Name the blood parasite species.
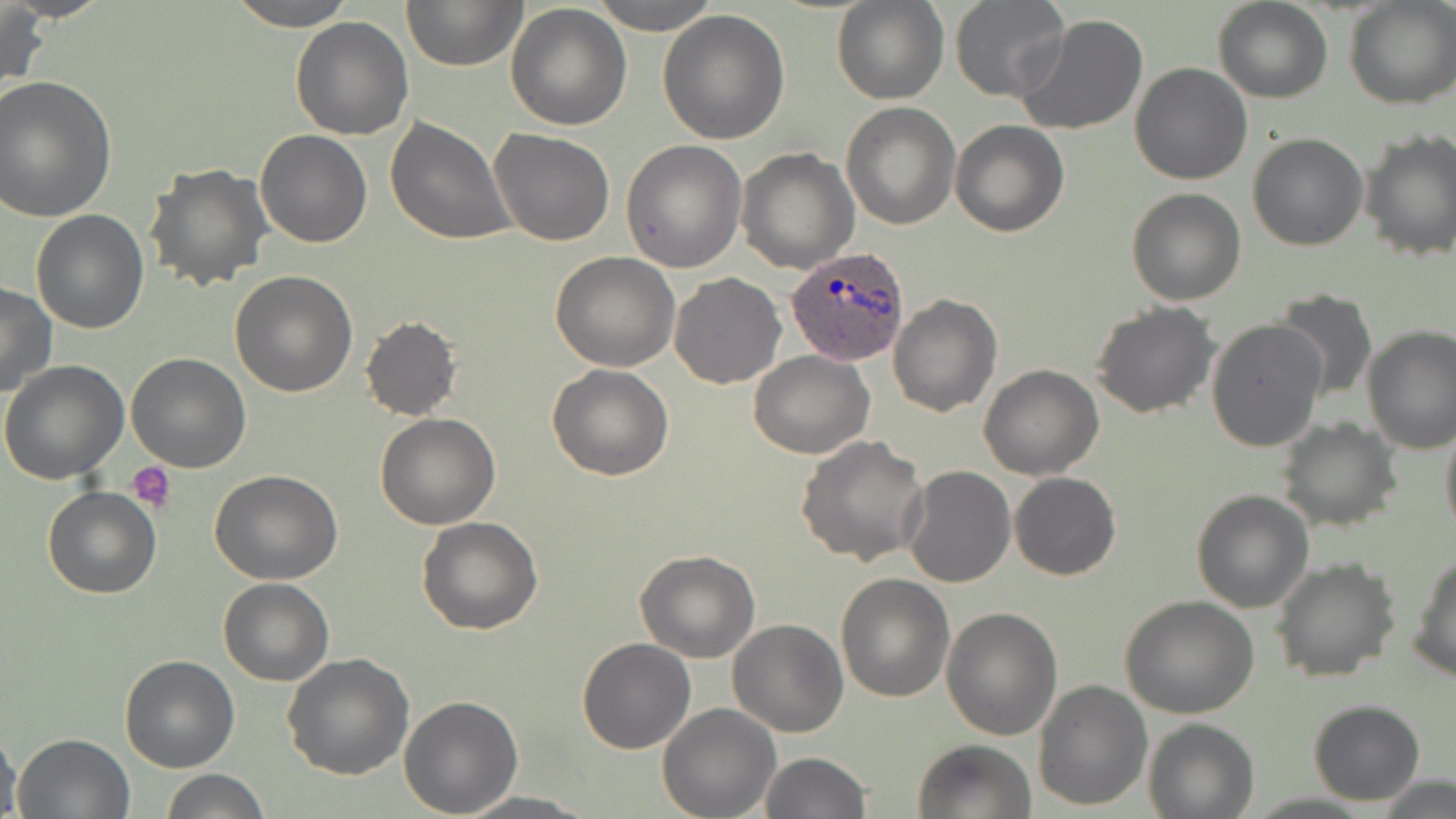
Plasmodium ovale.

Approximate bounding boxes as [x1, y1, x2, y2] in pixels. Plasmodium ovale-infected red blood cell locations: [787, 247, 909, 366]. Uninfected red blood cell locations: [228, 0, 358, 29], [402, 0, 525, 71], [589, 0, 722, 33], [1212, 0, 1333, 103], [831, 1, 949, 104], [949, 1, 1069, 101], [1344, 1, 1455, 109], [505, 3, 632, 132], [0, 4, 48, 97], [657, 9, 790, 143], [1012, 13, 1150, 136], [290, 16, 413, 140], [1131, 63, 1253, 185], [0, 75, 116, 223], [841, 102, 959, 229], [385, 117, 516, 245], [952, 121, 1069, 237], [490, 127, 615, 246], [255, 129, 372, 248], [1358, 131, 1456, 262], [1246, 133, 1369, 251], [621, 138, 748, 271], [735, 147, 858, 274], [142, 163, 273, 291], [1125, 187, 1246, 306], [30, 209, 150, 332], [549, 253, 681, 371], [229, 269, 357, 396], [668, 274, 785, 389], [0, 284, 56, 399], [1272, 289, 1377, 402], [888, 294, 1003, 417], [1090, 302, 1221, 419], [360, 316, 461, 421], [1207, 318, 1327, 453], [1362, 325, 1456, 454], [748, 350, 875, 458], [126, 353, 251, 473], [0, 358, 129, 484], [547, 364, 675, 480], [978, 365, 1104, 480], [375, 413, 502, 529], [1439, 416, 1456, 543], [1276, 417, 1402, 533], [795, 434, 930, 566], [901, 465, 1016, 587], [211, 470, 343, 584], [1009, 472, 1121, 581], [43, 487, 161, 598], [1190, 490, 1314, 612], [417, 517, 543, 635], [634, 549, 761, 663], [1409, 550, 1456, 682], [1271, 557, 1402, 682], [836, 572, 956, 702], [218, 578, 333, 686], [1119, 597, 1261, 718], [941, 606, 1064, 741], [728, 618, 849, 737], [576, 638, 697, 755], [282, 652, 415, 779], [117, 655, 239, 773], [1032, 678, 1152, 811], [398, 695, 524, 816], [1307, 699, 1427, 804], [658, 703, 781, 819], [1143, 718, 1258, 818], [0, 722, 22, 819], [12, 731, 136, 819], [911, 738, 1035, 819], [759, 751, 870, 819], [161, 768, 269, 819], [1374, 774, 1454, 819], [459, 792, 599, 817]. Platelet locations: [128, 461, 177, 513]. Light microscopy. Thin blood film. 1000x magnification. One field of a larger specimen. May-Grünwald-Giemsa stain. Image is 1456×819 pixels.